State the preparation type.
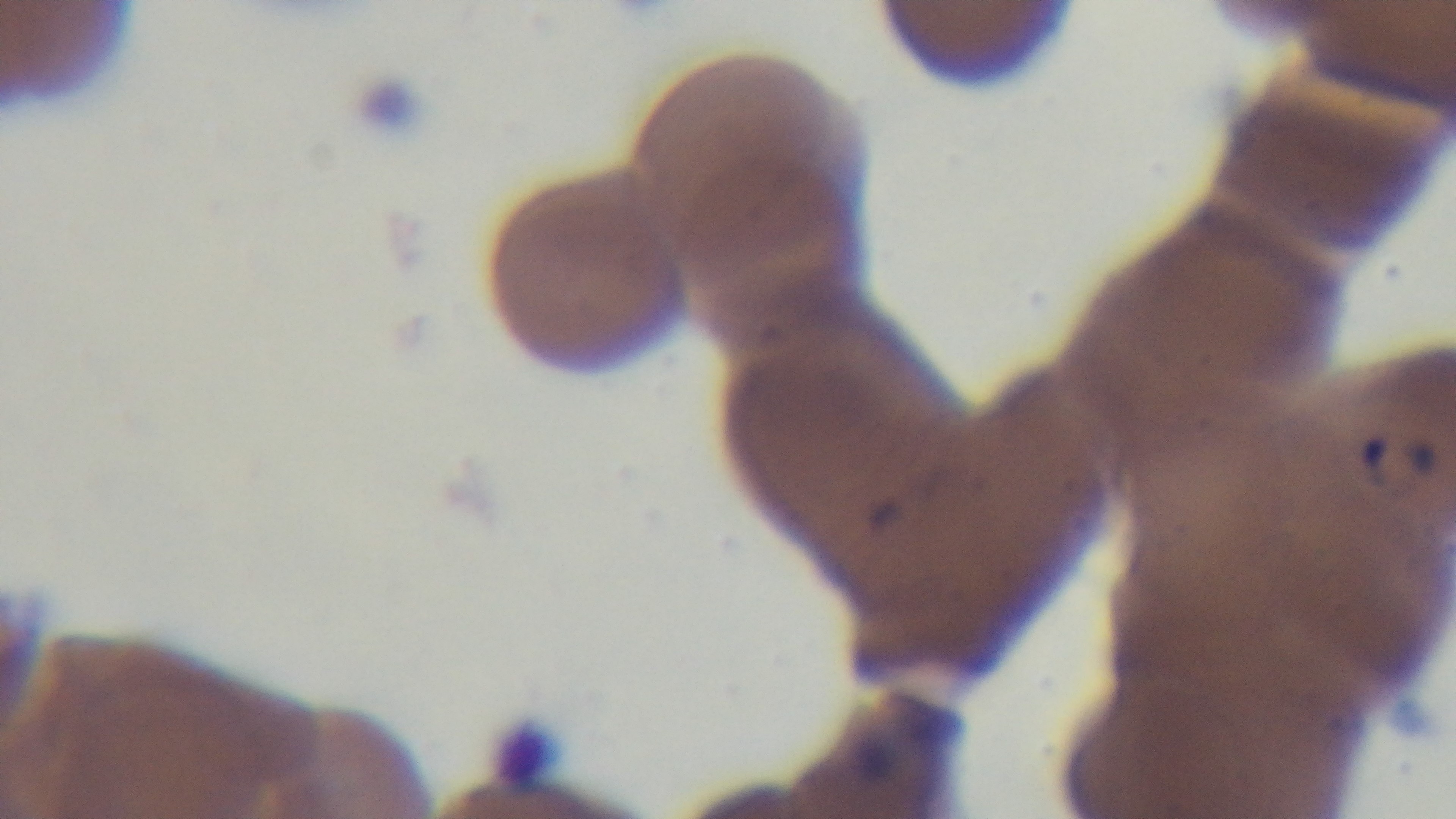

It is a thin blood film.

{
  "objective": "100x oil immersion",
  "modality": "light microscopy",
  "stain": "Giemsa",
  "capture": "mounted 4K digital camera",
  "field_of_view": "single",
  "malaria_status": "infected"
}